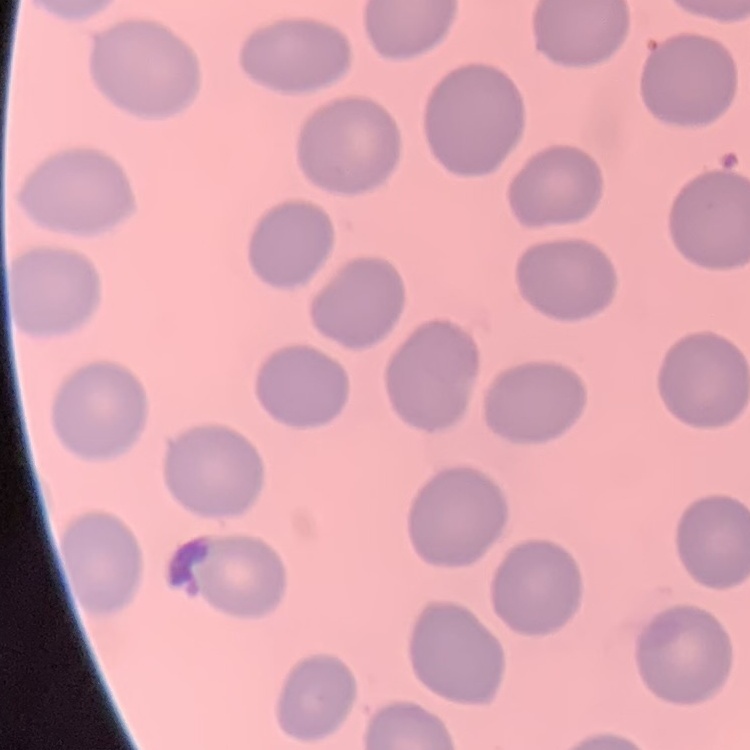
red blood cell morphology = no rouleaux formation
preparation = thin peripheral smear
stain = Field's or Giemsa
image type = one tile cut from a larger photomicrograph